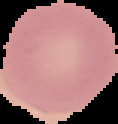
Malaria status: uninfected. Image is 118×124 pixels. From a thin blood film. Cell region segmented out of the field of view; the surrounding area is masked to black.